Give the extent of the malaria parasites you find, grouped by life-cycle stage — ring form, trophozoite, schizont, or gametocyte.
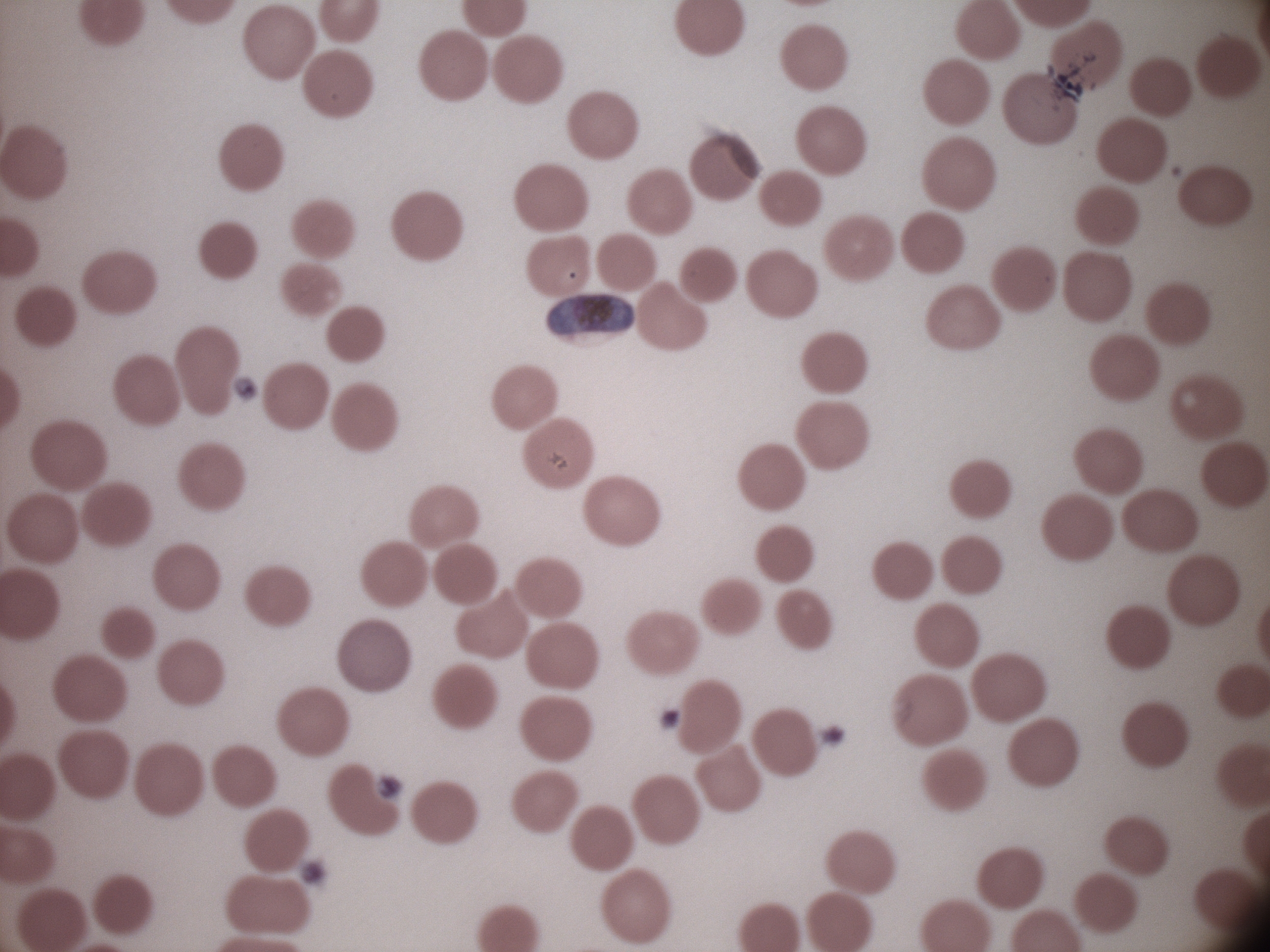
Approximate bounding boxes as (x1, y1, x2, y2) in pixels, from the source annotation, which is not necessarily exhaustive.
Gametocytes: (547, 293, 635, 335).

image_size: 1270×952 pixels
species: Plasmodium falciparum
field_of_view: one from this slide
microscope: Leica DM2000 with built-in camera
stain: Giemsa
magnification: 100x
preparation: thin blood smear